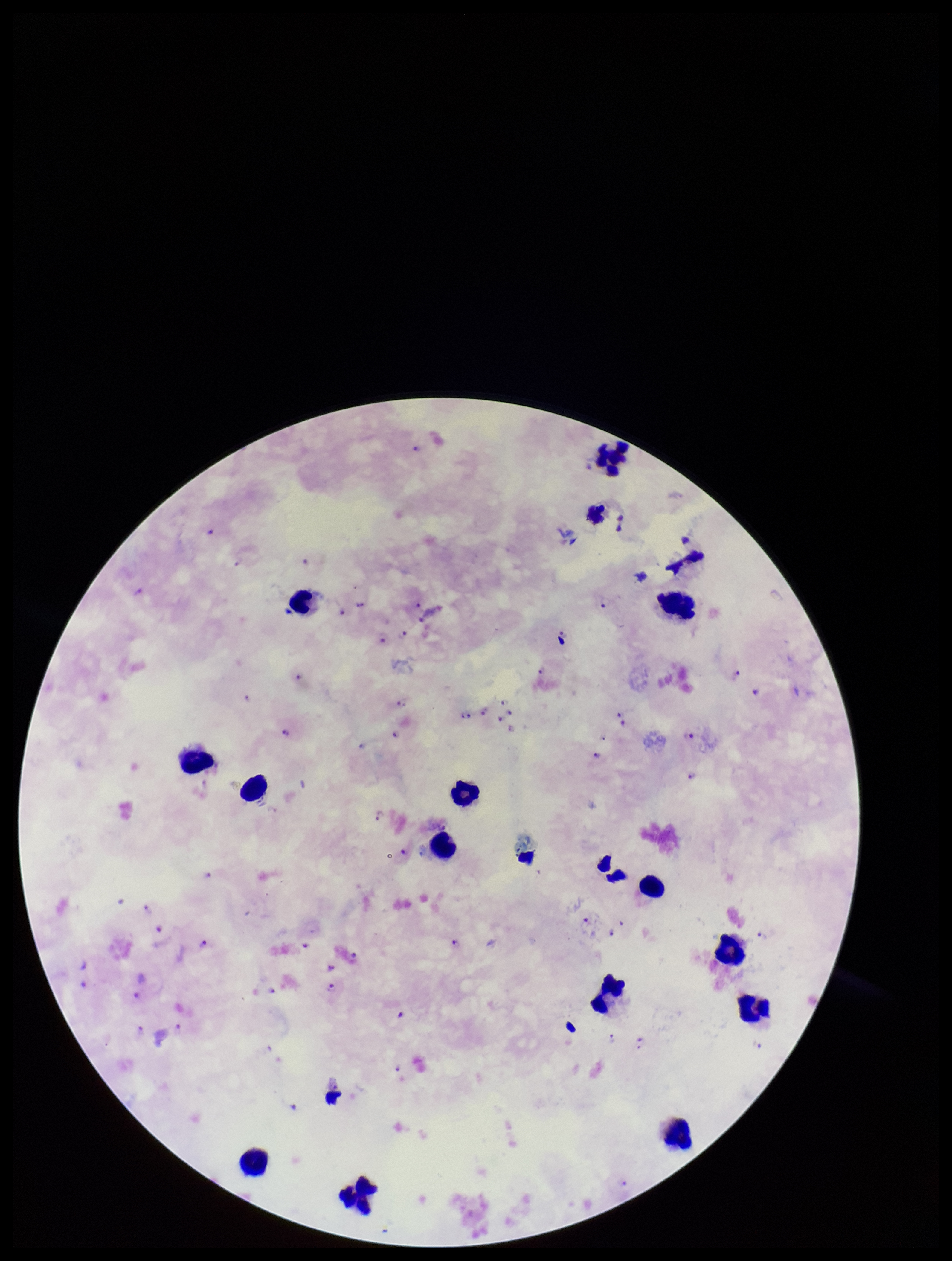
Summary:
  - Parasite count: 52
  - Species reported for this patient: Plasmodium falciparum
  - Leukocyte count: 15
  - Field of view: single
  - Image size: 952×1261 pixels
  - Preparation: thick smear
  - Patient malaria status: infected
  - Capture: smartphone photograph through the microscope eyepiece
  - Stain: Giemsa
  - Plasmodium parasites: detected